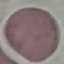
Summary:
  - Result: no malaria parasites seen
  - Stain: Giemsa
  - Capture: smartphone through the microscope eyepiece
  - Image type: cell patch, automatically extracted from a larger field of view and resized to 64 × 64 pixels
  - Preparation: thin smear